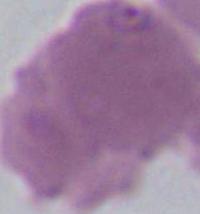
identification = red blood cell
magnification = 1000x
modality = photomicrograph